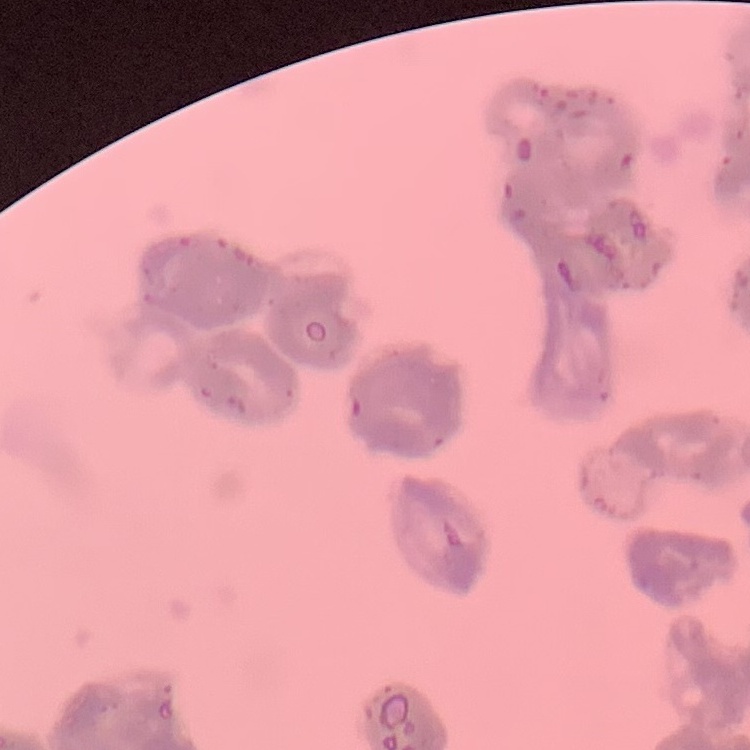

Summary:
  - Red blood cell morphology: rouleaux formation
  - Image type: one tile cut from a larger photomicrograph
  - Stain: Field's or Giemsa
  - Preparation: thin peripheral smear